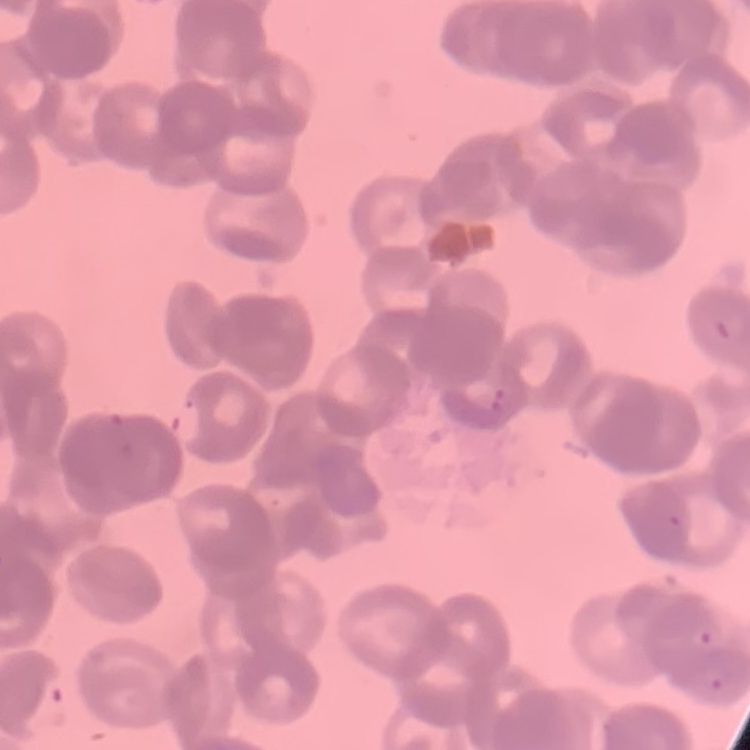
erythrocyte morphology = rouleaux formation
stain = Field's or Giemsa
image type = one tile cut from a larger photomicrograph
preparation = thin blood smear